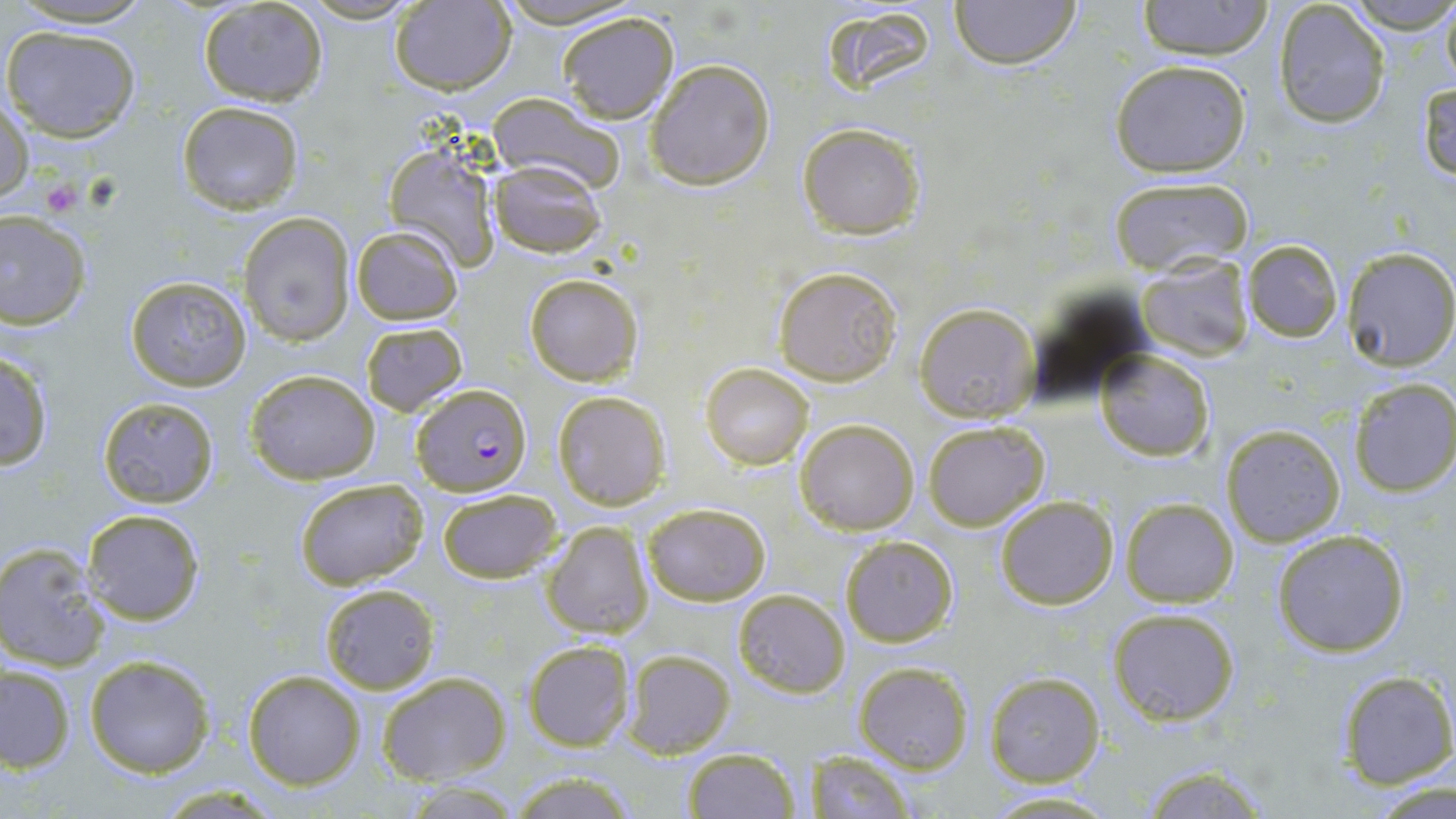
slide-level diagnosis = Plasmodium falciparum
preparation = thin blood smear
modality = optical microscopy
uninfected red blood cell locations = approximate bounding boxes as (x1, y1, x2, y2) in pixels: (4, 0, 157, 30), (948, 0, 1081, 69), (1136, 0, 1275, 59), (1346, 0, 1456, 36), (1440, 0, 1456, 94), (196, 1, 329, 107), (298, 1, 424, 24), (1272, 1, 1392, 129), (388, 2, 516, 93), (818, 4, 945, 100), (557, 11, 680, 123), (3, 23, 140, 142), (645, 58, 775, 190), (1110, 59, 1251, 178), (1416, 78, 1456, 184), (487, 93, 626, 195), (0, 94, 34, 206), (177, 100, 305, 214), (797, 123, 924, 238), (382, 137, 502, 272), (488, 159, 606, 259), (1108, 177, 1252, 275), (0, 210, 92, 330), (239, 212, 355, 346), (350, 225, 464, 325), (1243, 239, 1342, 343), (1340, 246, 1456, 370), (1135, 254, 1253, 362), (774, 267, 903, 386), (525, 274, 642, 386), (125, 275, 254, 390), (913, 302, 1042, 422), (361, 323, 466, 416), (0, 348, 55, 472), (1096, 350, 1214, 461), (701, 363, 813, 469), (246, 369, 382, 485), (1349, 378, 1456, 497), (552, 390, 672, 510), (98, 397, 219, 507), (796, 419, 920, 534), (923, 421, 1050, 532), (1220, 423, 1346, 547), (293, 475, 428, 589), (436, 488, 562, 584), (993, 495, 1119, 610), (1119, 498, 1239, 607), (642, 502, 772, 605), (80, 507, 206, 625), (541, 521, 653, 640), (1270, 529, 1410, 657), (839, 534, 958, 647), (0, 542, 112, 672), (318, 583, 440, 694), (732, 588, 850, 697), (1108, 606, 1241, 726), (521, 640, 633, 752), (622, 648, 736, 757), (84, 654, 215, 778), (854, 660, 974, 773), (1, 664, 76, 773), (242, 670, 365, 790), (983, 671, 1104, 786), (377, 672, 511, 785), (1335, 672, 1454, 788), (681, 746, 800, 818), (798, 752, 918, 817), (1134, 763, 1276, 819), (504, 771, 640, 818), (1369, 776, 1454, 816), (980, 790, 1128, 818)
stain = May-Grünwald-Giemsa
platelet locations = approximate bounding boxes as (x1, y1, x2, y2) in pixels: (40, 180, 83, 216)
magnification = 1000x
image size = 1456×819 pixels
Plasmodium falciparum-infected red blood cell locations = approximate bounding boxes as (x1, y1, x2, y2) in pixels: (411, 383, 531, 495)
field of view = one of a larger specimen